Locate every Plasmodium parasite.
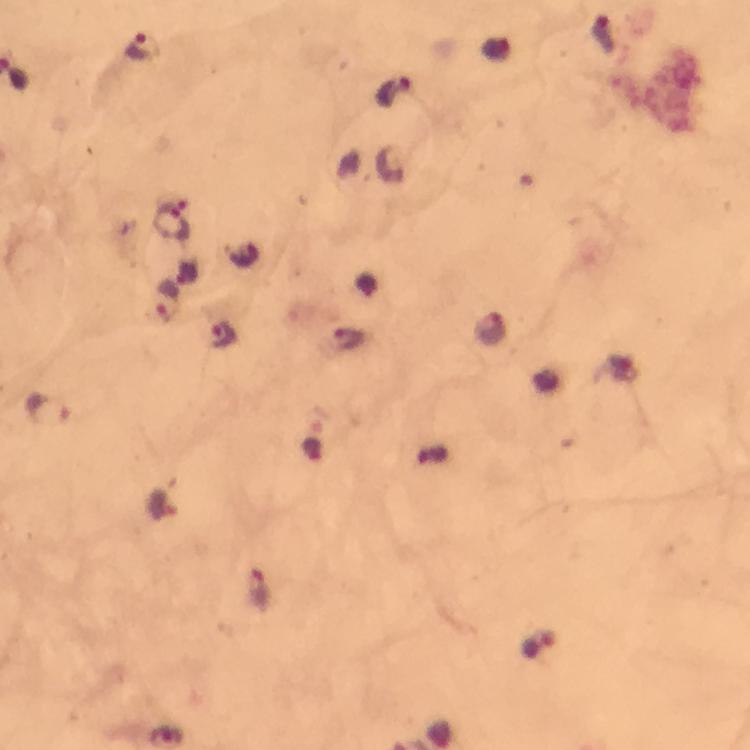

Approximate object centers, in pixels from the top-left corner.
Plasmodium parasites: (x=604, y=35), (x=142, y=47), (x=394, y=92), (x=171, y=223), (x=167, y=300), (x=489, y=329), (x=223, y=335), (x=347, y=341), (x=46, y=410), (x=162, y=506), (x=258, y=590), (x=537, y=645).

Thick smear. At 100x magnification. From a malaria diagnostic workup. Photographed with a smartphone mounted on the microscope. Immersion oil was used. Cropped region of a single field of view. Image is 750×750 pixels. Giemsa stain.